Give the position of each Plasmodium falciparum parasite with its life-cycle stage, each leukocyte, and any debris.
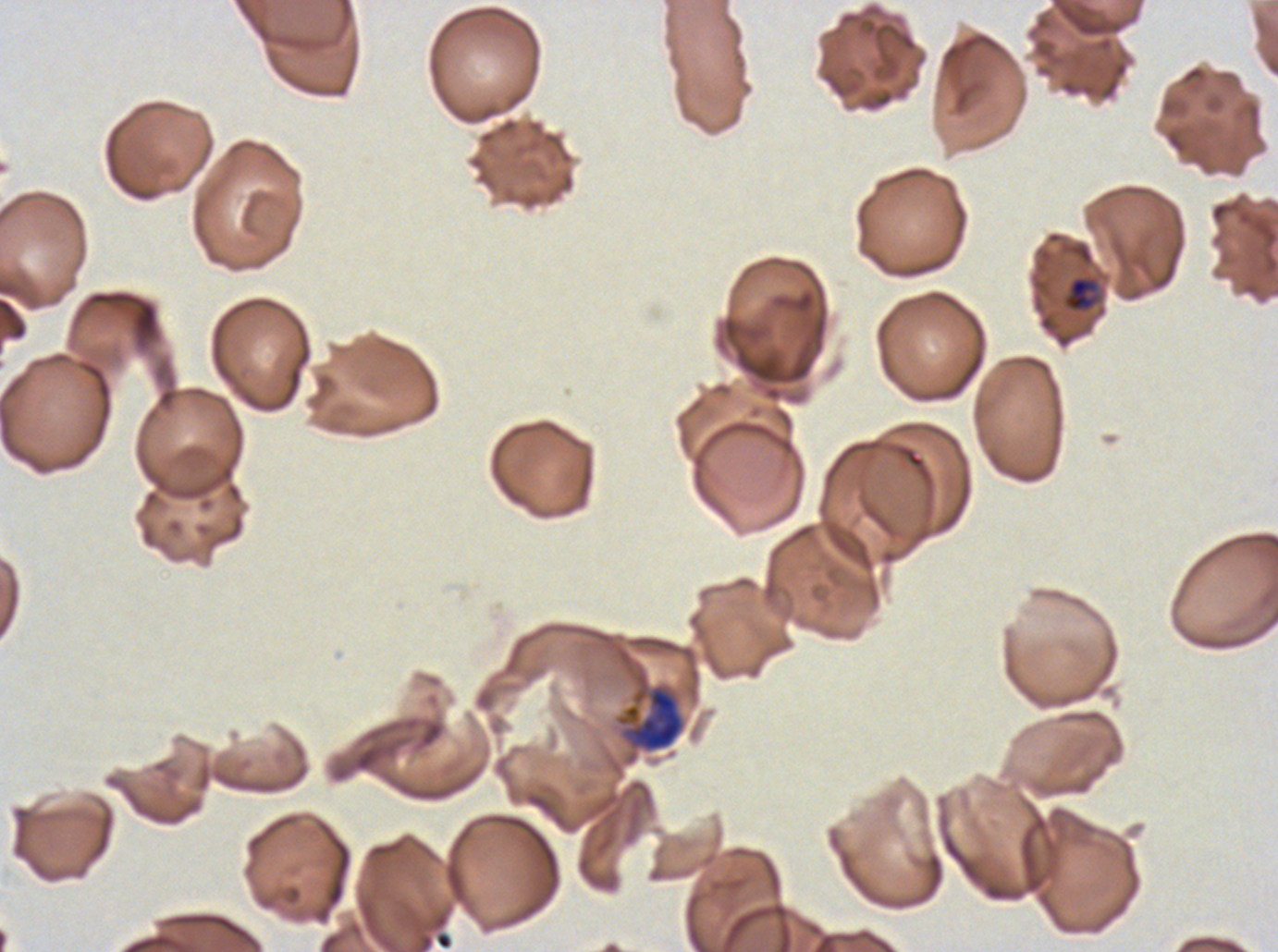
Approximate bounding rectangles given as corner coordinates in pixels from the top-left.
Mid trophozoites: (x1=1063, y1=275, x2=1099, y2=312).
Late trophozoites: (x1=615, y1=673, x2=685, y2=753).
No rings, late-ring/early-trophozoite forms, early schizonts, late schizonts, segmenters, gametocytes, leukocytes, or debris observed.

field of view = sub-image separated from a larger composite
specimen = Plasmodium falciparum cultured ex vivo for 24 to 48 hours, from a patient in The Gambia
image size = 1278×952 pixels
stain = Giemsa
preparation = thin blood smear
life-cycle stages observed = mid trophozoite, late trophozoite